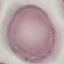

result: no malaria parasites seen
preparation: thin blood smear
capture: smartphone through the microscope eyepiece
image_type: automatically extracted cell patch, resized to 64 × 64 pixels
stain: Giemsa